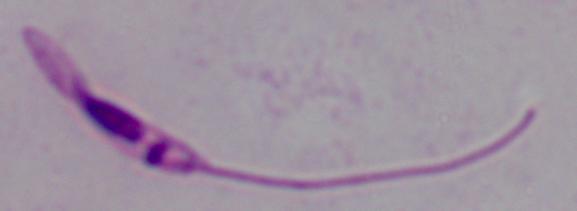

A Leishmania parasite is shown. Captured at 1000x magnification. Photomicrograph.